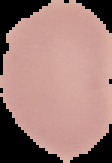
{
  "malaria_status": "uninfected",
  "image_size": "112×163 pixels",
  "image_type": "cell region segmented out of the field of view; surrounding area masked to black",
  "preparation": "thin blood film"
}